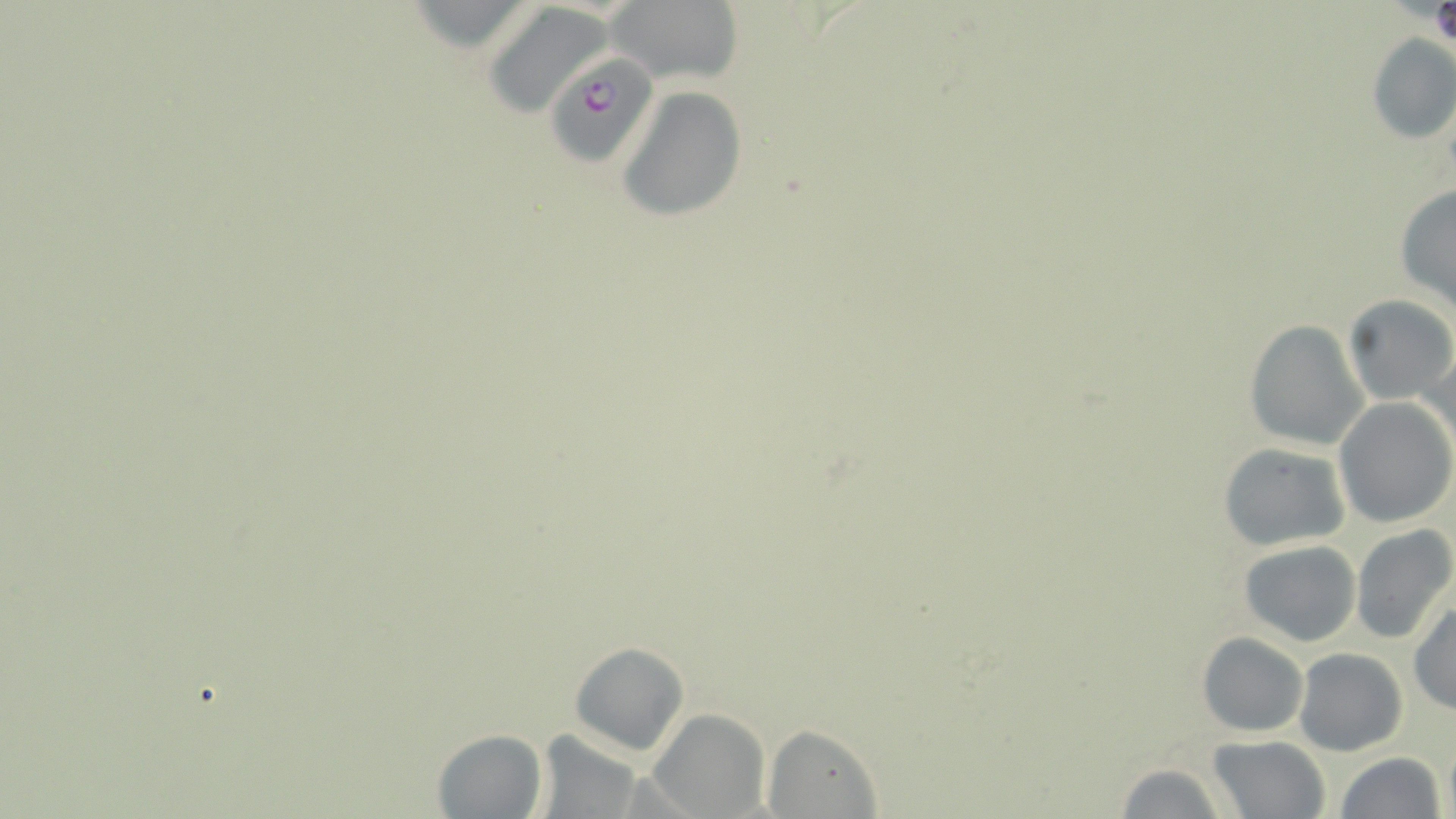

slide_level_diagnosis: Plasmodium falciparum
uninfected_red_blood_cell_locations: 'approximate bounding boxes as (x1, y1, x2, y2) in pixels: (607, 1, 743, 86), (481, 3, 618, 119), (1366, 31, 1456, 145), (617, 86, 747, 223), (1394, 182, 1456, 313), (1341, 294, 1455, 406), (1244, 321, 1370, 451), (1419, 344, 1456, 463), (1334, 398, 1455, 527), (1217, 442, 1353, 550), (1351, 525, 1456, 646), (1239, 540, 1362, 646), (1409, 602, 1456, 715), (1198, 632, 1308, 737), (569, 640, 691, 755), (1294, 648, 1408, 757), (648, 708, 768, 818), (763, 725, 883, 819), (432, 728, 547, 817), (534, 730, 646, 818), (1207, 735, 1330, 818), (1336, 752, 1446, 819), (1110, 762, 1232, 818)'
magnification: 1000x
preparation: thin blood film
image_size: 1456×819 pixels
plasmodium_falciparum_infected_red_blood_cell_locations: 'approximate bounding boxes as (x1, y1, x2, y2) in pixels: (551, 55, 665, 166)'
modality: light microscopy
field_of_view: single
stain: May-Grünwald-Giemsa